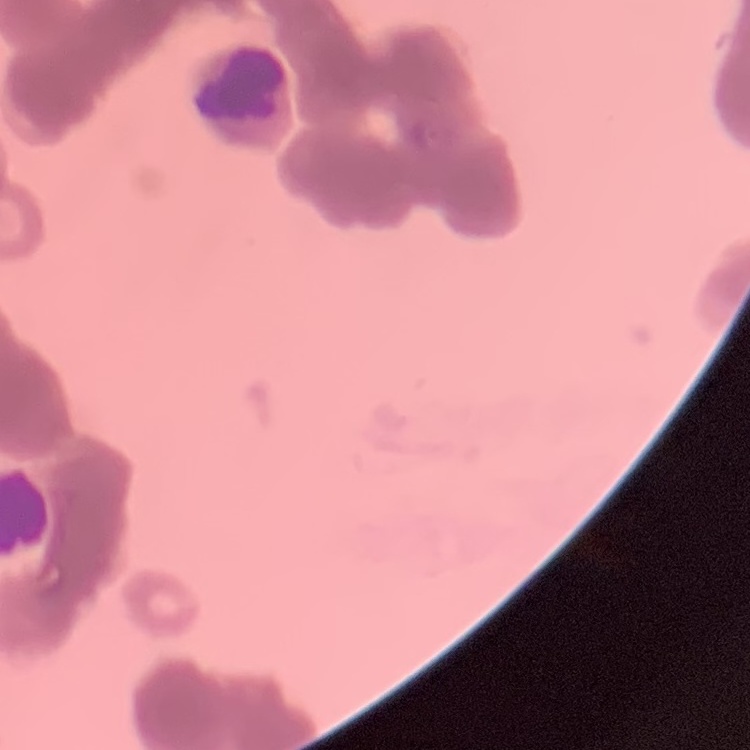

erythrocyte_morphology: rouleaux formation
stain: Field's or Giemsa
image_type: square crop of a larger photomicrograph
preparation: thin blood smear